Assess this cell for malaria.
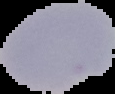

It is parasitized.

image type = segmented cell region on a black background
preparation = thin blood film
image size = 115×94 pixels